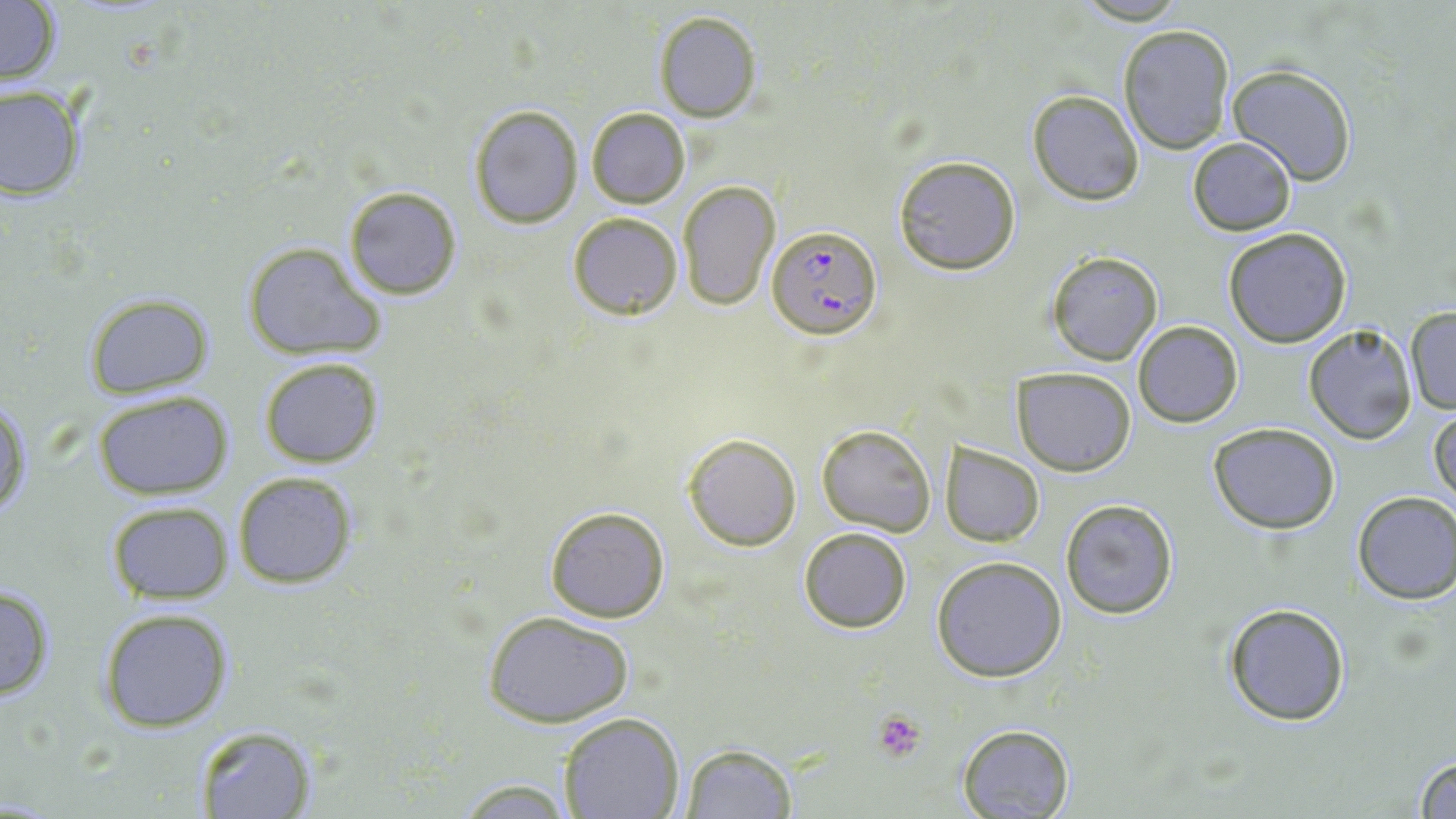
Approximate bounding boxes as (x1,y1)-(x2,y2) corner pairs in pixels. Plasmodium falciparum-infected red blood cell locations: (766,224)-(882,340). Uninfected red blood cell locations: (0,1)-(61,87), (654,11)-(762,122), (1117,23)-(1235,154), (1227,64)-(1356,186), (0,86)-(85,201), (1027,90)-(1144,206), (468,103)-(584,228), (586,108)-(689,207), (1188,138)-(1296,236), (893,156)-(1021,275), (676,180)-(781,312), (343,185)-(463,299), (566,211)-(683,319), (1222,227)-(1353,348), (242,242)-(386,361), (1046,252)-(1163,365), (81,293)-(216,400), (1405,306)-(1456,414), (1133,320)-(1243,427), (1302,323)-(1417,445), (260,356)-(383,467), (1011,366)-(1137,476), (92,391)-(234,499), (0,397)-(33,521), (1430,406)-(1455,514), (1208,422)-(1340,533), (817,423)-(935,536), (684,432)-(801,550), (940,442)-(1044,547), (232,471)-(358,590), (1351,492)-(1456,605), (1061,498)-(1179,620), (105,501)-(233,605), (544,505)-(671,624), (797,527)-(913,633), (932,556)-(1067,682), (0,581)-(57,703), (1222,601)-(1352,726), (96,606)-(234,733), (484,610)-(634,729), (558,713)-(684,819), (955,723)-(1074,819), (193,725)-(318,818), (679,743)-(797,818), (1411,751)-(1456,819), (447,777)-(582,816). Platelet locations: (872,709)-(928,762). Slide-level diagnosis: Plasmodium falciparum. May-Grünwald-Giemsa-stained preparation. Single field of view. Thin blood film. Captured at 1000x magnification. Image is 1456×819 pixels. Light microscopy.